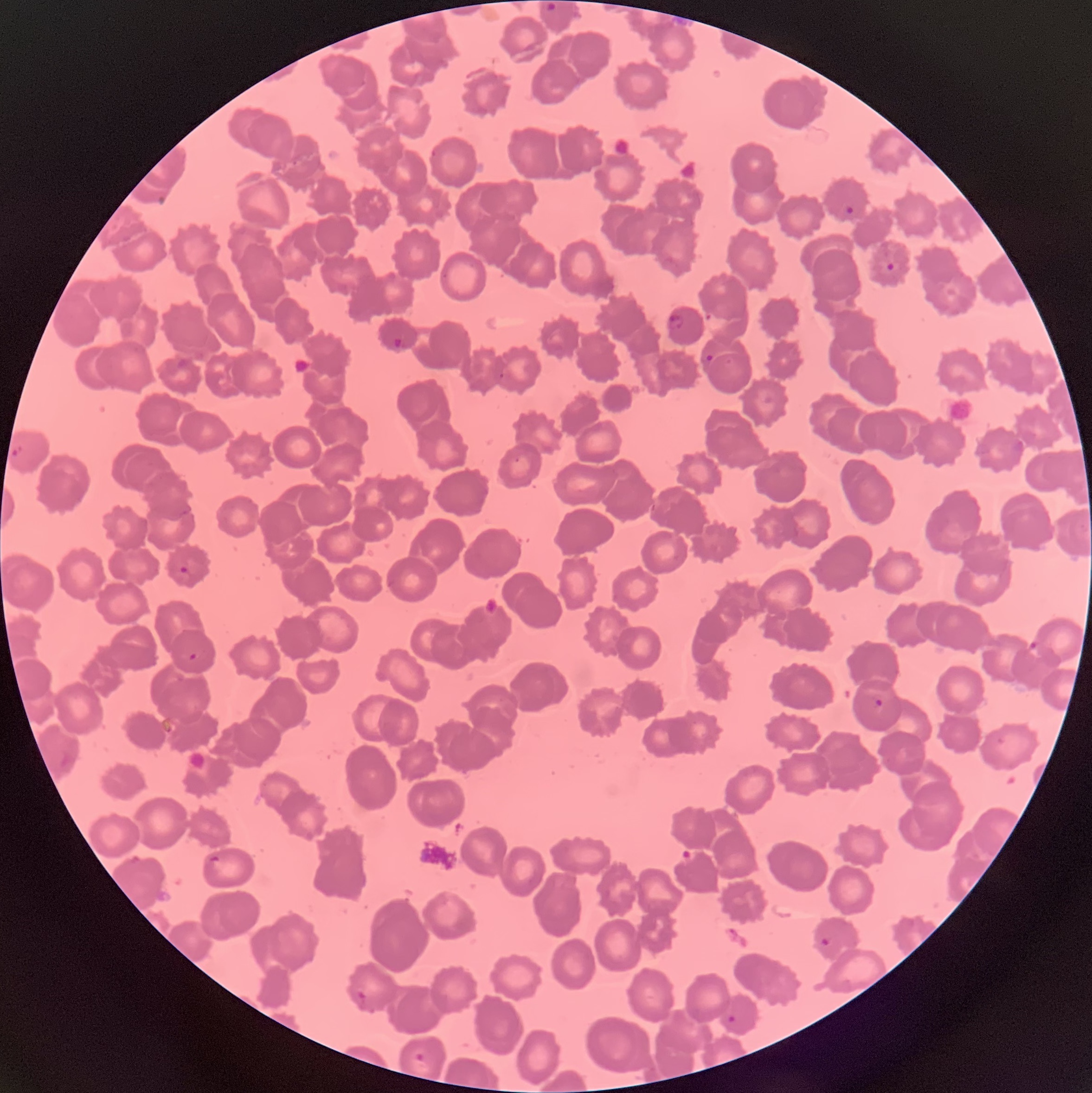
Approximate bounding boxes as (x1, y1, x2, y2) in pixels. Plasmodium parasite locations: (547, 3, 556, 11), (841, 207, 854, 220), (886, 262, 895, 270), (705, 311, 713, 323), (668, 315, 685, 332), (392, 336, 405, 350), (706, 353, 714, 362), (11, 445, 24, 457), (178, 565, 192, 576), (1029, 640, 1038, 650), (188, 651, 198, 662), (874, 697, 884, 707), (820, 937, 832, 948), (356, 990, 368, 1008), (727, 1015, 735, 1023), (413, 1052, 427, 1063). Thin blood smear. Optical microscopy. The red blood cells show rouleaux formation. Image is 1092×1093 pixels.